Identify the parasite.
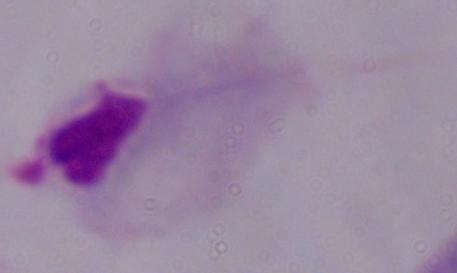
A trichomonad.

Captured at 1000x magnification. Micrograph.